Comment on the morphology of the erythrocytes.
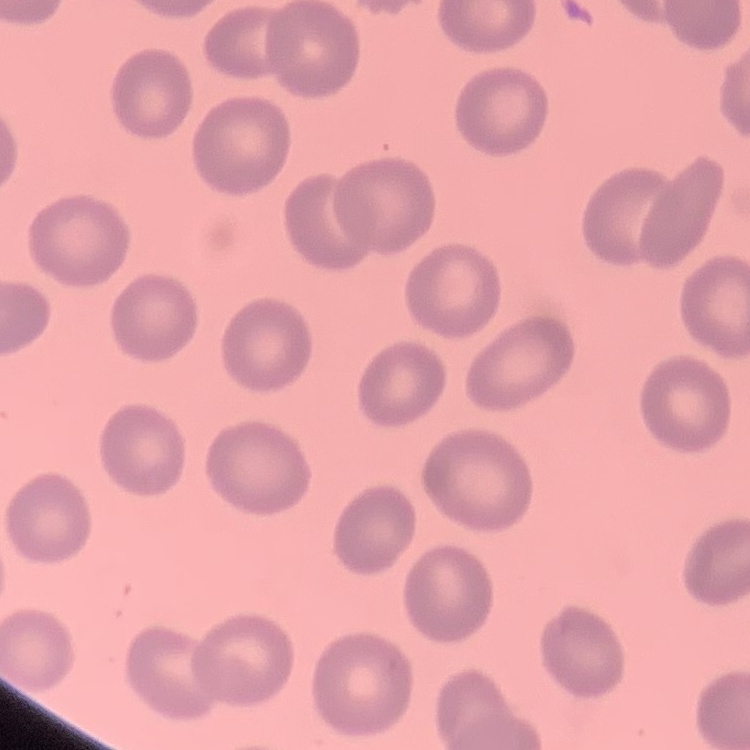
No rouleaux formation.

image type = one tile cut from a larger photomicrograph
stain = Field's or Giemsa
preparation = thin blood film